Describe the morphology of the red blood cells.
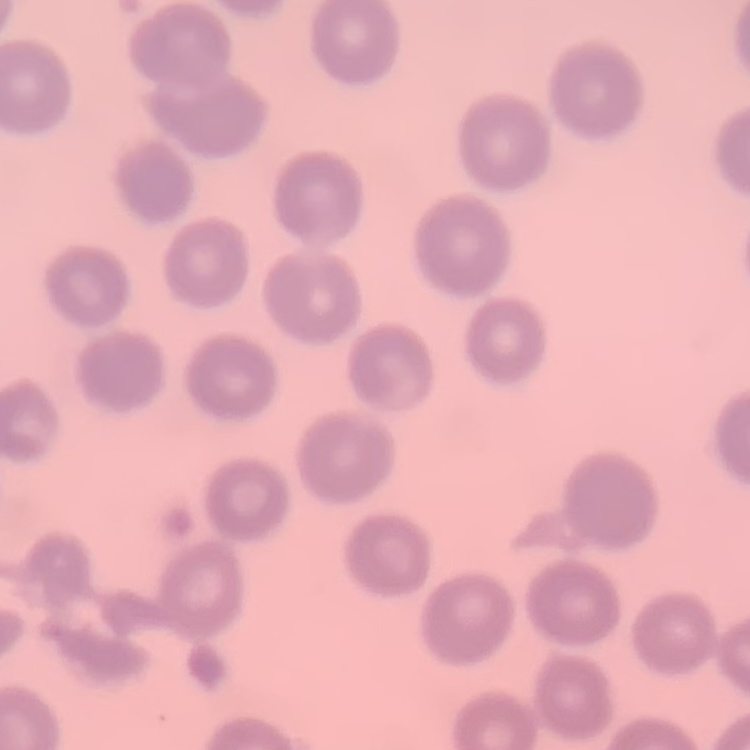
They show no rouleaux formation.

Summary:
  - Image type: square crop of a larger photomicrograph
  - Stain: Field's or Giemsa
  - Preparation: thin blood film